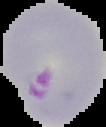
From a thin blood film. Image is 106×127 pixels. Result: malaria parasites detected. Cell region segmented out of the field of view; the surrounding area is masked to black.